Classify this cell by malaria status.
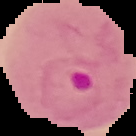
Parasitized.

image type = cell region segmented out of the field of view; surrounding area masked to black
image size = 136×136 pixels
preparation = thin blood smear